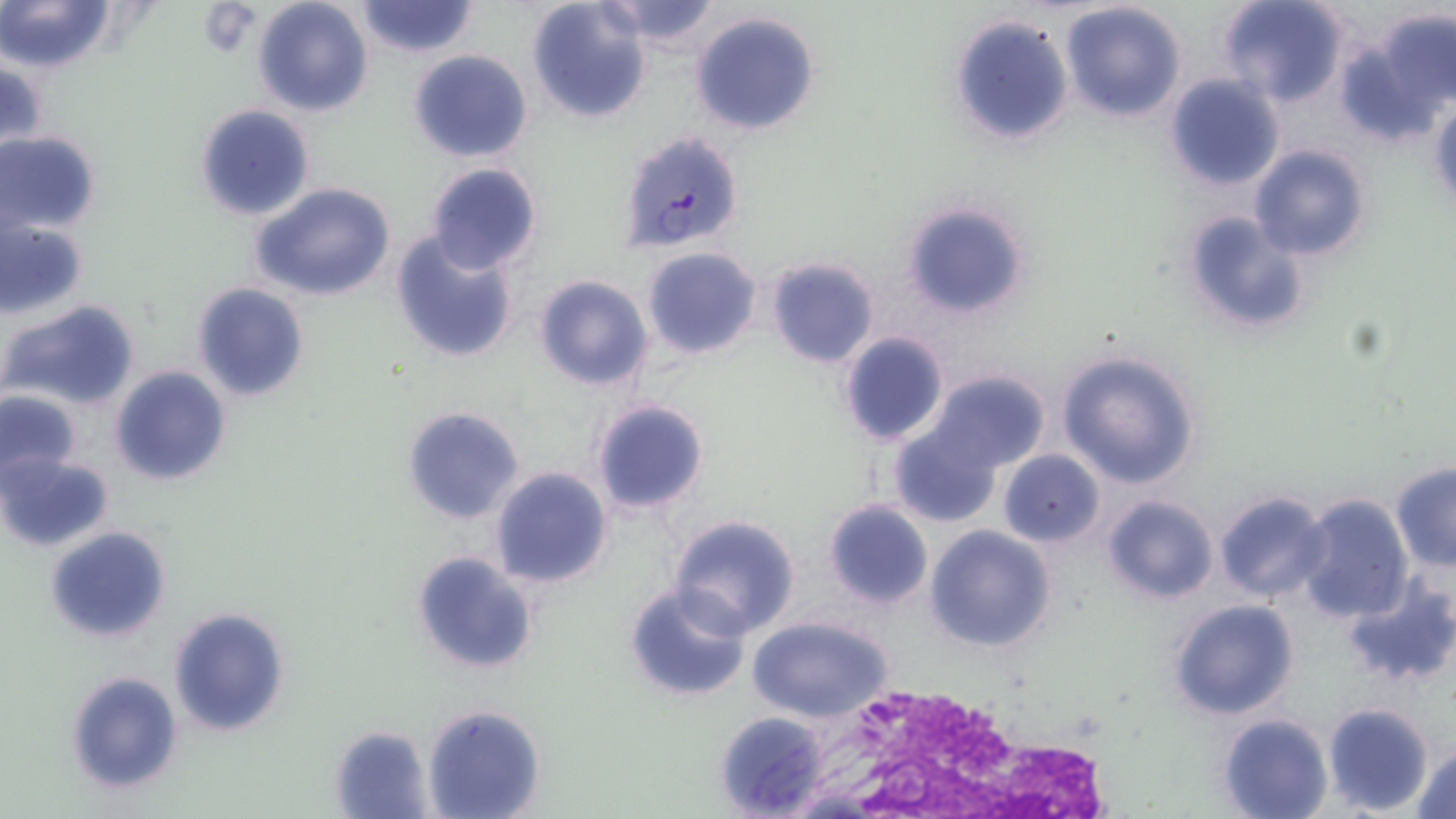
slide-level diagnosis = Plasmodium falciparum
stain = May-Grünwald-Giemsa
Plasmodium falciparum-infected red blood cell locations = approximate bounding boxes as [x1, y1, x2, y2] in pixels: [621, 132, 745, 252]
magnification = 1000x
preparation = thin blood smear
white blood cell locations = approximate bounding boxes as [x1, y1, x2, y2] in pixels: [796, 677, 1101, 815]
image size = 1456×819 pixels
modality = optical microscopy
field of view = one of a larger specimen
uninfected red blood cell locations = approximate bounding boxes as [x1, y1, x2, y2] in pixels: [2, 0, 115, 74], [252, 0, 373, 118], [526, 0, 652, 122], [598, 0, 722, 50], [1218, 0, 1349, 106], [354, 1, 480, 57], [1060, 1, 1186, 121], [1363, 9, 1456, 130], [689, 11, 820, 137], [948, 15, 1075, 147], [407, 49, 533, 163], [1163, 73, 1285, 191], [191, 104, 315, 221], [0, 131, 101, 235], [1248, 144, 1372, 262], [424, 161, 543, 274], [251, 182, 396, 303], [900, 200, 1031, 321], [1180, 207, 1311, 337], [1, 218, 89, 318], [389, 230, 520, 365], [642, 247, 762, 361], [764, 257, 881, 369], [533, 274, 652, 390], [191, 282, 309, 402], [4, 298, 141, 413], [837, 331, 951, 448], [1056, 348, 1203, 488], [110, 365, 232, 485], [926, 368, 1052, 472], [0, 389, 81, 483], [588, 397, 711, 518], [402, 405, 526, 526], [888, 424, 1003, 527], [997, 449, 1104, 547], [0, 451, 112, 551], [1390, 464, 1455, 573], [489, 466, 613, 589], [1213, 491, 1331, 604], [1294, 494, 1415, 624], [1101, 495, 1218, 604], [822, 500, 933, 609], [668, 515, 801, 639], [923, 525, 1058, 652], [44, 526, 171, 645], [410, 551, 538, 675], [1344, 576, 1456, 690], [622, 582, 751, 705], [1166, 599, 1300, 721], [168, 606, 290, 738], [748, 617, 891, 722], [65, 670, 183, 794], [1322, 702, 1434, 816], [422, 703, 545, 818], [713, 710, 831, 817], [1217, 713, 1333, 819], [330, 725, 433, 817], [1410, 743, 1456, 818]
platelet locations = approximate bounding boxes as [x1, y1, x2, y2] in pixels: [197, 5, 258, 56]